Identify the preparation type.
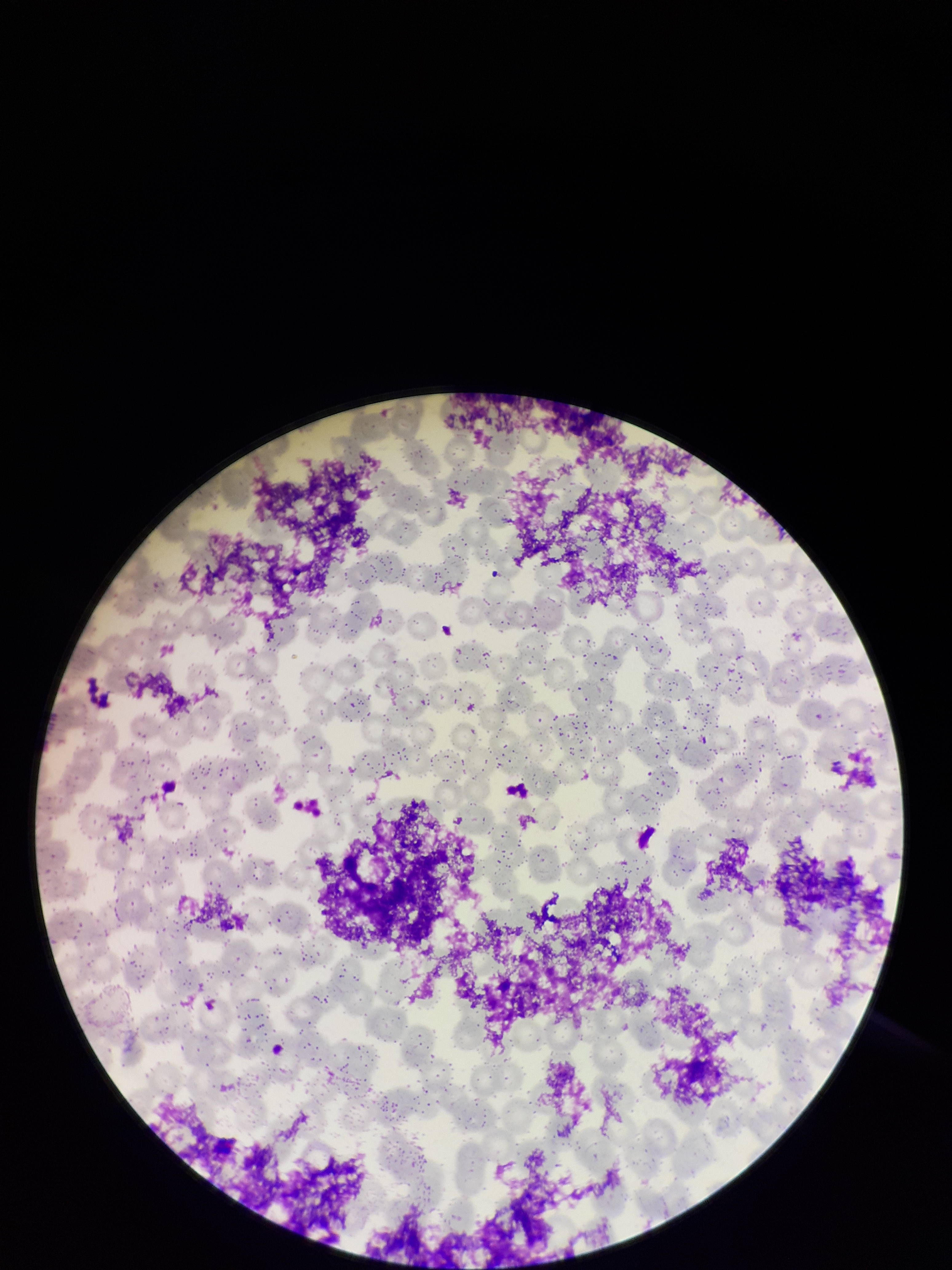
A thin smear.

Image is 952×1270 pixels. Smartphone photograph taken through the eyepiece of a microscope. Red blood cell count: 296. Parasitized red blood cells: none seen. Single field of view. Giemsa stain. Patient malaria status: negative. Parasitized red blood cell count: 0.